Point out malaria parasites and leukocytes.
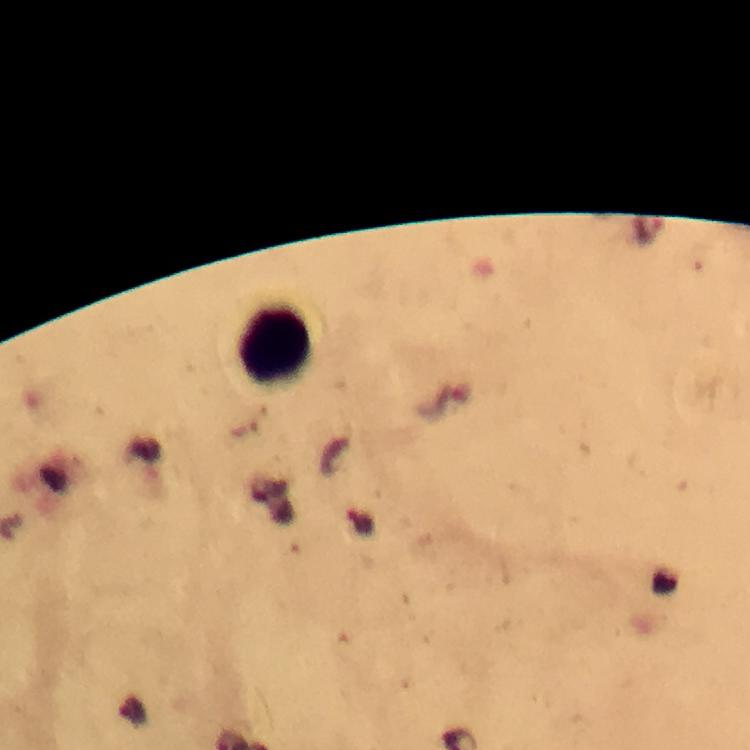

No malaria parasites seen.
Approximate object centers, in pixels from the top-left corner.
Leukocytes: (x=273, y=346).

{
  "context": "from a malaria diagnostic workup",
  "immersion_oil": "applied",
  "image_size": "750×750 pixels",
  "magnification": "100x",
  "cropped_from": "one field of view",
  "stain": "Giemsa",
  "preparation": "thick blood smear",
  "capture": "smartphone photograph through a microscope"
}